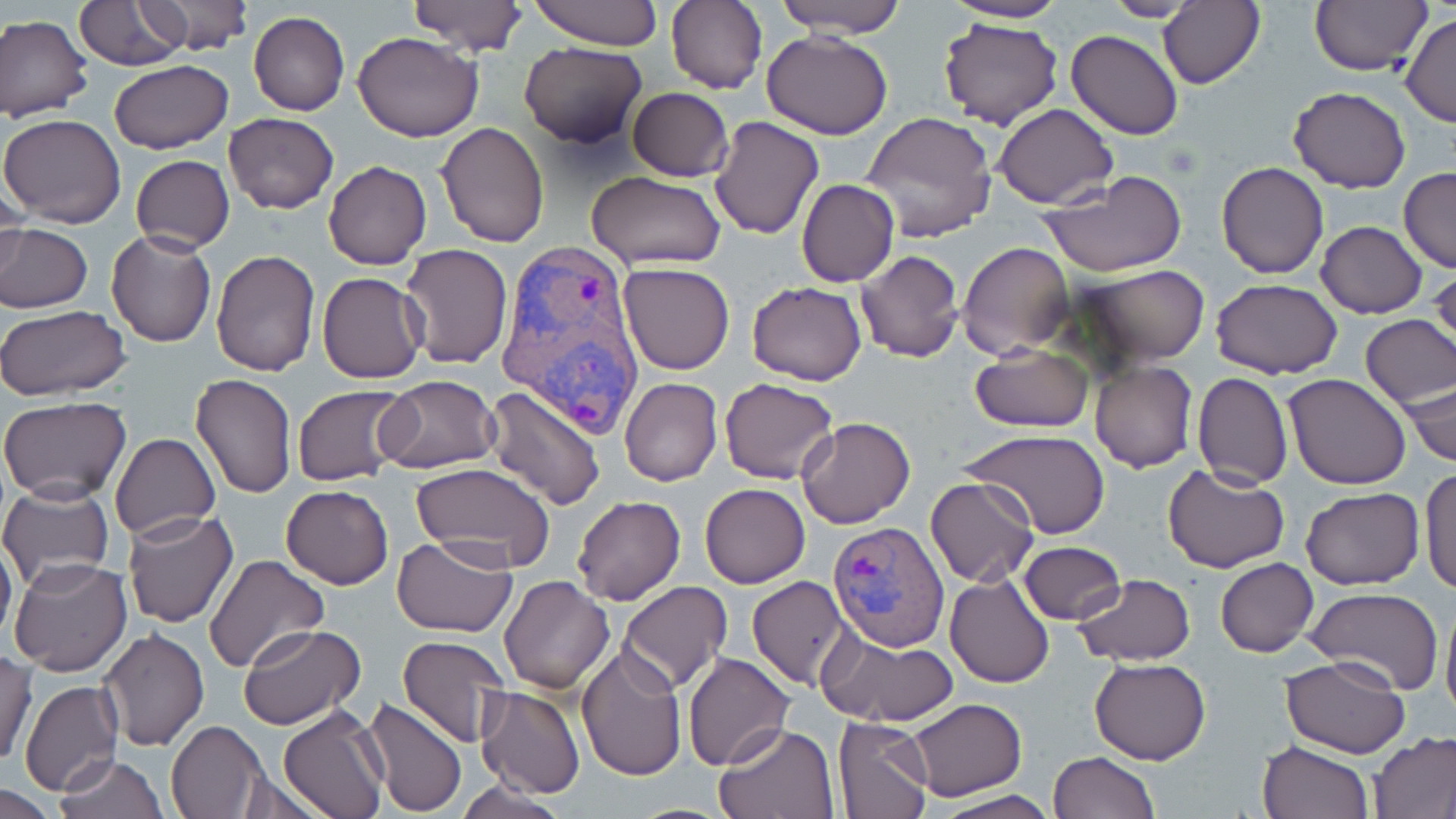

{
  "slide_level_diagnosis": "Plasmodium vivax",
  "image_size": "1456×819 pixels",
  "magnification": "1000x",
  "uninfected_red_blood_cell_locations": "approximate bounding boxes as named x1/y1/x2/y2 corners in pixels: (x1=136, y1=0, x2=253, y2=57), (x1=528, y1=0, x2=661, y2=49), (x1=772, y1=0, x2=910, y2=38), (x1=1101, y1=0, x2=1201, y2=22), (x1=1159, y1=0, x2=1264, y2=90), (x1=1308, y1=0, x2=1432, y2=76), (x1=406, y1=1, x2=529, y2=55), (x1=666, y1=1, x2=768, y2=94), (x1=944, y1=1, x2=1072, y2=25), (x1=74, y1=2, x2=190, y2=70), (x1=247, y1=10, x2=348, y2=117), (x1=1401, y1=12, x2=1456, y2=128), (x1=0, y1=14, x2=94, y2=123), (x1=939, y1=17, x2=1065, y2=131), (x1=762, y1=30, x2=892, y2=140), (x1=1066, y1=30, x2=1184, y2=141), (x1=354, y1=31, x2=484, y2=142), (x1=519, y1=41, x2=648, y2=148), (x1=109, y1=58, x2=234, y2=155), (x1=1288, y1=86, x2=1410, y2=193), (x1=627, y1=87, x2=733, y2=182), (x1=992, y1=105, x2=1117, y2=206), (x1=861, y1=111, x2=1000, y2=246), (x1=0, y1=112, x2=127, y2=228), (x1=223, y1=112, x2=338, y2=213), (x1=708, y1=115, x2=824, y2=240), (x1=435, y1=121, x2=550, y2=247), (x1=132, y1=154, x2=235, y2=254), (x1=324, y1=160, x2=431, y2=269), (x1=1216, y1=161, x2=1328, y2=279), (x1=1400, y1=167, x2=1456, y2=273), (x1=586, y1=171, x2=729, y2=273), (x1=1039, y1=173, x2=1189, y2=277), (x1=797, y1=178, x2=899, y2=288), (x1=0, y1=179, x2=27, y2=284), (x1=1316, y1=221, x2=1427, y2=318), (x1=0, y1=222, x2=93, y2=313), (x1=106, y1=228, x2=216, y2=348), (x1=956, y1=241, x2=1074, y2=360), (x1=399, y1=243, x2=515, y2=368), (x1=210, y1=250, x2=320, y2=375), (x1=855, y1=250, x2=964, y2=363), (x1=618, y1=262, x2=735, y2=376), (x1=1074, y1=265, x2=1209, y2=366), (x1=316, y1=272, x2=427, y2=384), (x1=1210, y1=278, x2=1343, y2=380), (x1=746, y1=281, x2=867, y2=385), (x1=0, y1=305, x2=131, y2=400), (x1=1359, y1=313, x2=1455, y2=411), (x1=970, y1=343, x2=1093, y2=431), (x1=1089, y1=362, x2=1197, y2=472), (x1=189, y1=372, x2=297, y2=498), (x1=1192, y1=373, x2=1292, y2=489), (x1=373, y1=374, x2=501, y2=475), (x1=1283, y1=374, x2=1411, y2=490), (x1=1405, y1=374, x2=1455, y2=470), (x1=620, y1=377, x2=723, y2=487), (x1=719, y1=378, x2=839, y2=485), (x1=291, y1=385, x2=412, y2=486), (x1=485, y1=386, x2=607, y2=511), (x1=0, y1=398, x2=130, y2=502), (x1=796, y1=418, x2=916, y2=530), (x1=964, y1=429, x2=1110, y2=539), (x1=110, y1=433, x2=220, y2=540), (x1=410, y1=463, x2=556, y2=572), (x1=1162, y1=464, x2=1288, y2=572), (x1=1419, y1=466, x2=1456, y2=597), (x1=925, y1=476, x2=1039, y2=587), (x1=699, y1=482, x2=811, y2=589), (x1=280, y1=484, x2=393, y2=589), (x1=0, y1=485, x2=116, y2=589), (x1=1300, y1=487, x2=1424, y2=592), (x1=573, y1=494, x2=686, y2=605), (x1=120, y1=509, x2=238, y2=629), (x1=0, y1=532, x2=17, y2=649), (x1=391, y1=534, x2=518, y2=638), (x1=1018, y1=541, x2=1126, y2=624), (x1=204, y1=555, x2=329, y2=675), (x1=8, y1=557, x2=131, y2=677), (x1=1215, y1=558, x2=1319, y2=657), (x1=945, y1=573, x2=1055, y2=687), (x1=498, y1=574, x2=615, y2=694), (x1=1073, y1=574, x2=1196, y2=667), (x1=748, y1=576, x2=854, y2=689), (x1=620, y1=581, x2=732, y2=694), (x1=1304, y1=588, x2=1443, y2=695), (x1=1440, y1=589, x2=1456, y2=731), (x1=239, y1=626, x2=366, y2=728), (x1=818, y1=626, x2=959, y2=728), (x1=99, y1=627, x2=208, y2=752), (x1=396, y1=635, x2=514, y2=751), (x1=576, y1=642, x2=687, y2=781), (x1=683, y1=651, x2=793, y2=769), (x1=1, y1=652, x2=37, y2=766), (x1=1089, y1=657, x2=1212, y2=765), (x1=1280, y1=657, x2=1412, y2=758), (x1=19, y1=680, x2=124, y2=793), (x1=477, y1=687, x2=585, y2=798), (x1=362, y1=698, x2=468, y2=817), (x1=906, y1=698, x2=1028, y2=801), (x1=278, y1=704, x2=390, y2=819), (x1=832, y1=716, x2=934, y2=818), (x1=165, y1=720, x2=268, y2=818), (x1=714, y1=722, x2=840, y2=817), (x1=1367, y1=733, x2=1456, y2=818), (x1=1256, y1=740, x2=1374, y2=819), (x1=1049, y1=750, x2=1159, y2=818), (x1=54, y1=754, x2=170, y2=819), (x1=227, y1=772, x2=338, y2=818), (x1=455, y1=778, x2=569, y2=819), (x1=0, y1=785, x2=62, y2=817), (x1=925, y1=790, x2=1061, y2=819)",
  "plasmodium_vivax_infected_red_blood_cell_locations": "approximate bounding boxes as named x1/y1/x2/y2 corners in pixels: (x1=495, y1=240, x2=646, y2=441), (x1=827, y1=521, x2=951, y2=651)",
  "field_of_view": "single",
  "preparation": "thin blood smear",
  "stain": "May-Grünwald-Giemsa",
  "modality": "light microscopy"
}